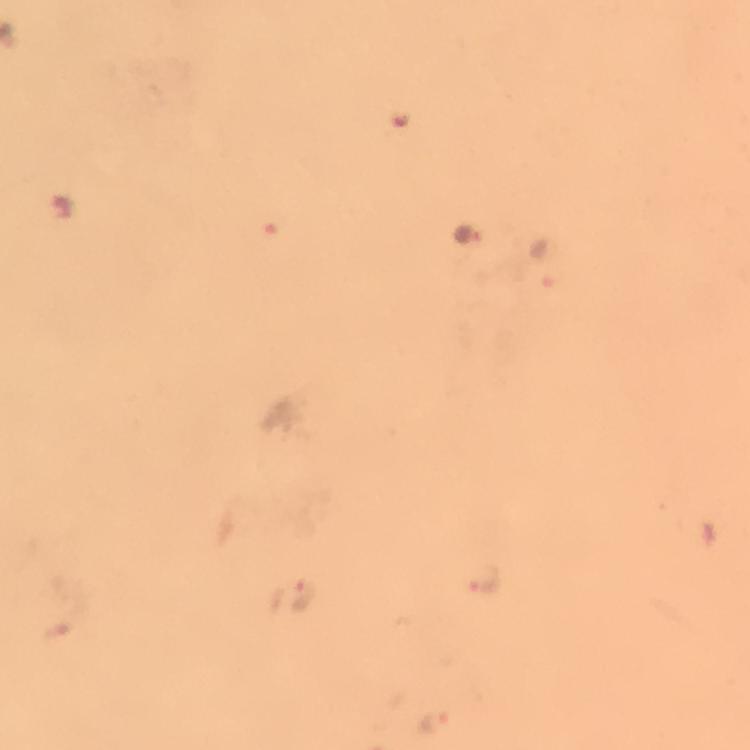 Approximate object centers, in pixels from the top-left corner. Malaria parasite locations: (x=545, y=259), (x=483, y=582), (x=291, y=596), (x=436, y=720). Immersion oil applied. From a diagnostic examination for malaria. Image is 750×750 pixels. Thick smear. 100x magnification. Photographed with a smartphone mounted on the microscope. A crop from one field of view. Giemsa-stained preparation.